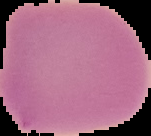

{
  "preparation": "thin blood film",
  "malaria_status": "uninfected",
  "image_size": "151×136 pixels",
  "image_type": "cell region segmented out of the field of view; surrounding area masked to black"
}